Classify this cell by malaria status.
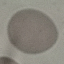

It is uninfected.

Cell patch, automatically extracted from a larger field of view and resized to 64 × 64 pixels. Thin blood smear. Giemsa stain. Acquired by smartphone through the microscope eyepiece.